Name the cell type shown.
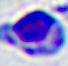

This is a leukocyte.

Photomicrograph. Captured at 400x magnification.